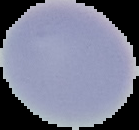 From a thin blood film. Cell region segmented out of the field of view; the surrounding area is masked to black. Image is 139×130 pixels. Malaria status: uninfected.